Classify this cell by malaria status.
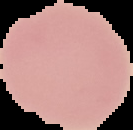
It is uninfected.

From a thin blood smear. Segmented cell region on a black background. Image is 133×130 pixels.